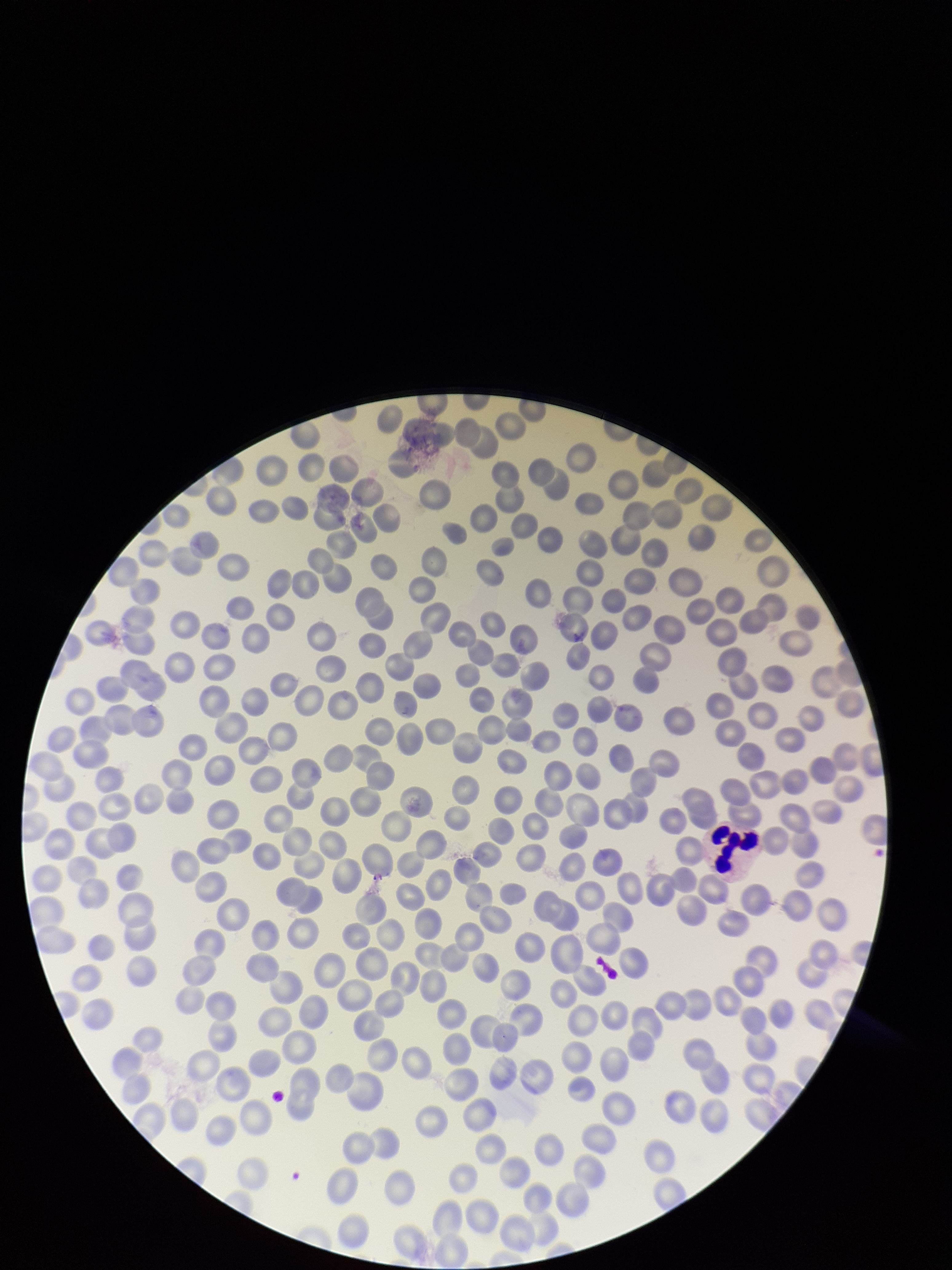
Summary:
  - Red blood cell count: 282
  - Image size: 952×1270 pixels
  - Parasitized red blood cell count: 0
  - Field of view: single
  - Parasitized red blood cells: none seen
  - Preparation: thin blood smear
  - Patient malaria status: negative
  - Stain: Giemsa
  - Capture: smartphone photograph through the microscope eyepiece